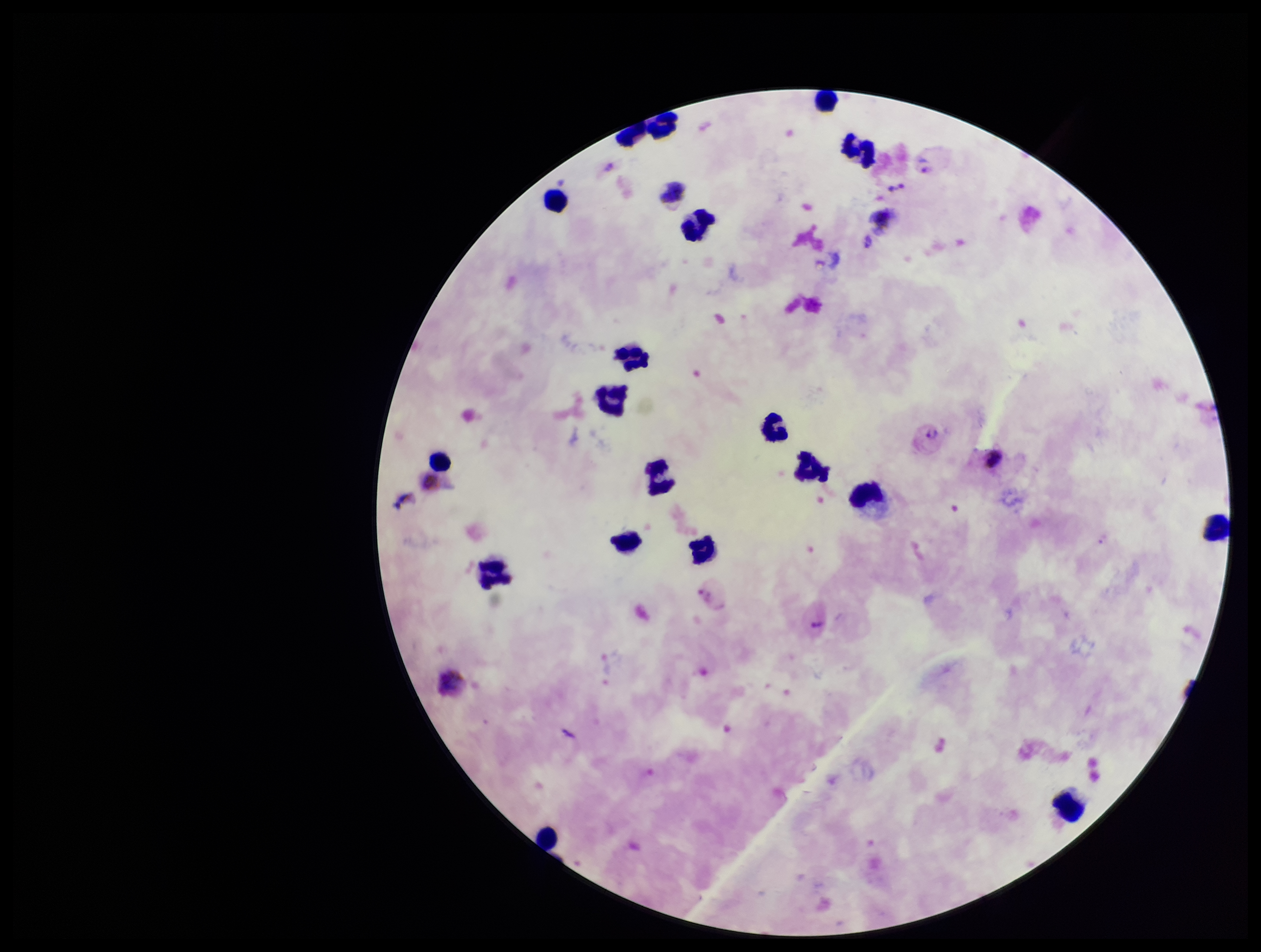
Image is 1261×952 pixels. Stained with Giemsa. Leukocyte count: 19. Plasmodium parasites: detected. Single field of view. Photographed through the microscope eyepiece with a smartphone camera. Species reported for this patient: Plasmodium vivax. Parasite count: 3. Patient malaria status: infected. Preparation: thick blood smear.